Give the preparation type.
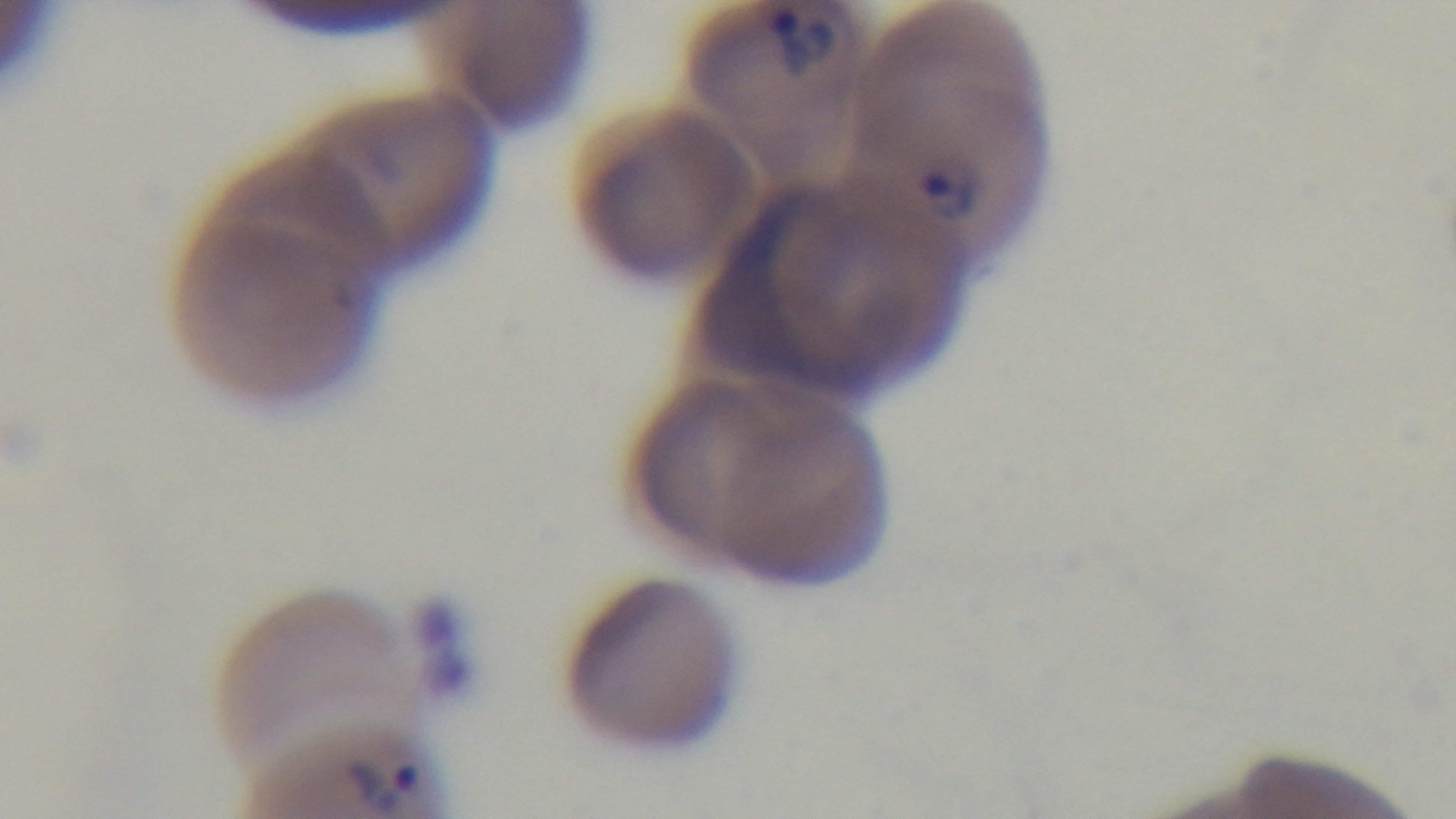
Thin.

Captured with a mounted 4K digital camera. Photomicrograph. Malaria status: infected. Single field of view. Giemsa stain. 100x oil-immersion objective.